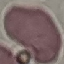

Result: negative for malaria parasites. Cell patch, automatically extracted from a larger field of view and resized to 64 × 64 pixels. Thin smear of blood. Photographed with a smartphone camera at the microscope eyepiece. Giemsa stain.